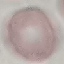 Result: negative for malaria parasites. Photographed with a smartphone camera at the microscope eyepiece. Automatically extracted cell patch, resized to 64 × 64 pixels. Giemsa stain. Thin blood smear.